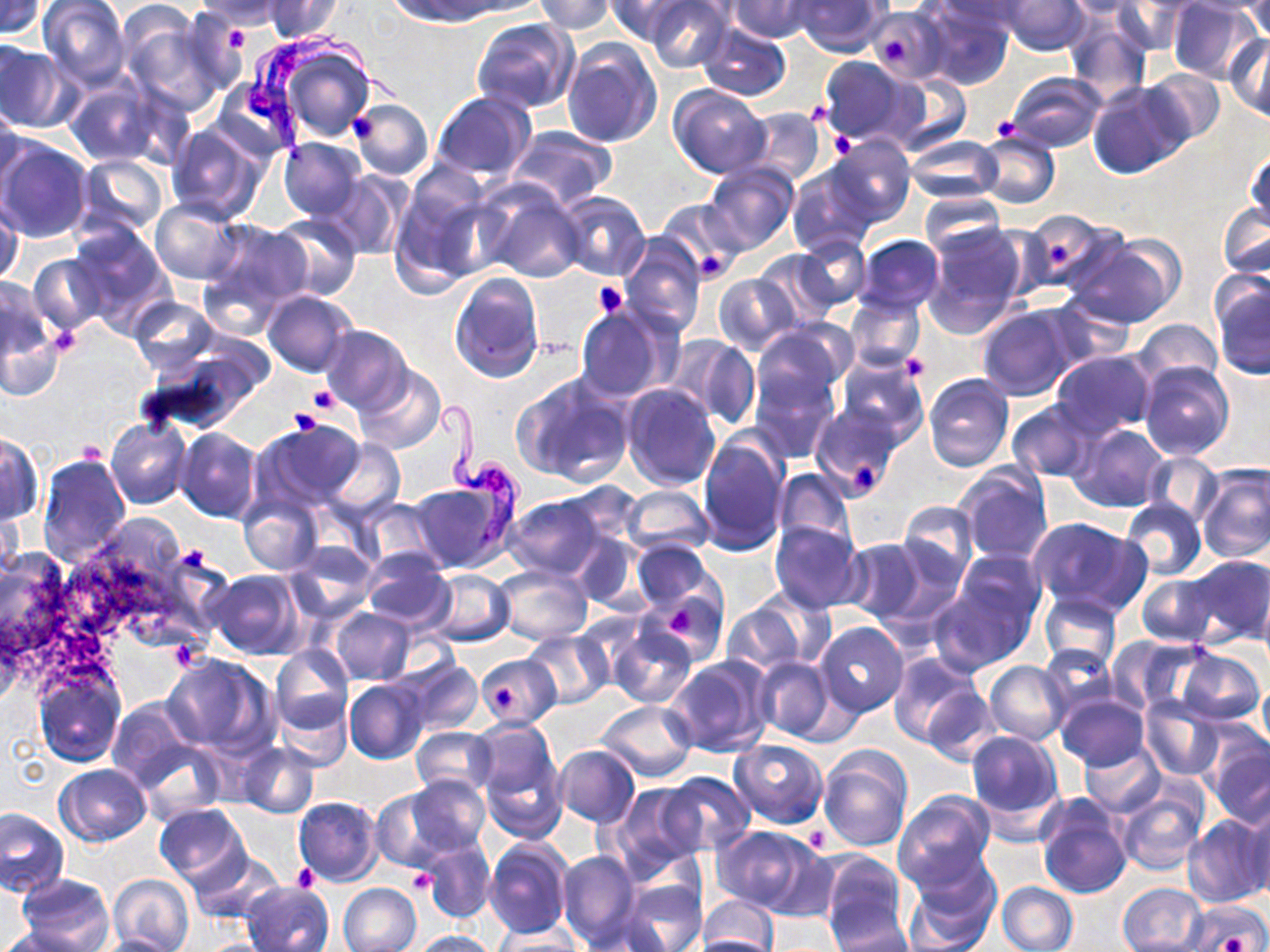

Summary:
  - Coordinate format: approximate bounding boxes as (x1, y1, x2, y2) in pixels
  - Platelet locations: (219, 20, 251, 51), (881, 34, 909, 66), (347, 111, 381, 143), (989, 116, 1021, 141), (829, 131, 857, 159), (1048, 243, 1072, 268), (696, 250, 729, 282), (593, 280, 629, 318), (48, 321, 85, 362), (902, 355, 930, 381), (307, 385, 342, 414), (288, 407, 323, 439), (77, 440, 104, 465), (853, 459, 885, 498), (178, 543, 211, 576), (665, 607, 699, 638), (495, 688, 517, 709), (801, 824, 832, 853), (292, 863, 320, 890), (407, 869, 437, 893), (1222, 932, 1247, 950)
  - Uninfected red blood cell locations: (0, 0, 49, 40), (38, 0, 130, 89), (264, 0, 344, 42), (453, 0, 547, 18), (534, 0, 617, 35), (605, 0, 693, 45), (644, 0, 733, 72), (730, 0, 818, 42), (794, 0, 888, 56), (933, 0, 1028, 38), (997, 0, 1090, 55), (1057, 0, 1149, 19), (1166, 0, 1265, 85), (1182, 0, 1270, 16), (1240, 0, 1270, 41), (191, 1, 290, 29), (392, 1, 499, 24), (1111, 1, 1189, 56), (116, 2, 207, 97), (918, 2, 1014, 90), (174, 8, 251, 96), (867, 9, 945, 82), (1062, 12, 1152, 103), (8, 16, 122, 123), (471, 18, 579, 113), (697, 22, 792, 100), (1226, 35, 1270, 122), (267, 39, 375, 143), (562, 39, 662, 148), (0, 42, 73, 131), (816, 55, 921, 148), (1139, 67, 1227, 147), (887, 72, 971, 156), (1006, 72, 1108, 153), (66, 76, 159, 167), (213, 77, 303, 163), (1087, 82, 1188, 180), (668, 83, 772, 178), (431, 91, 536, 184), (349, 99, 433, 179), (0, 106, 25, 195), (738, 107, 826, 185), (165, 122, 267, 226), (509, 126, 614, 208), (976, 132, 1059, 209), (826, 134, 914, 226), (0, 136, 92, 243), (905, 136, 1002, 204), (279, 137, 366, 221), (1245, 147, 1269, 233), (77, 155, 170, 236), (702, 163, 799, 255), (786, 167, 875, 256), (322, 171, 408, 259), (387, 180, 496, 293), (478, 180, 587, 283), (919, 189, 1006, 255), (556, 191, 651, 280), (0, 198, 22, 289), (150, 200, 241, 284), (657, 200, 745, 278), (1218, 201, 1269, 283), (1019, 210, 1122, 296), (270, 214, 360, 301), (201, 218, 312, 322), (67, 220, 174, 335), (921, 222, 1028, 336), (618, 234, 706, 336), (854, 234, 944, 315), (1068, 234, 1183, 329), (794, 235, 871, 312), (754, 249, 840, 326), (27, 252, 105, 337), (450, 272, 544, 381), (713, 273, 798, 355), (1210, 275, 1270, 380), (1, 278, 61, 382), (263, 290, 358, 377), (845, 294, 925, 373), (1044, 294, 1137, 369), (128, 297, 217, 374), (575, 305, 672, 403), (977, 305, 1078, 400), (1132, 319, 1222, 387), (321, 325, 413, 413), (750, 325, 850, 415), (668, 335, 758, 429), (135, 337, 272, 437), (834, 349, 928, 443), (1050, 350, 1157, 439), (1138, 362, 1234, 460), (750, 363, 838, 461), (356, 365, 446, 454), (923, 373, 1015, 472), (516, 374, 634, 487), (620, 383, 721, 491), (1006, 398, 1100, 483), (810, 404, 903, 501), (106, 417, 192, 511), (253, 419, 367, 512), (1069, 423, 1169, 513), (176, 427, 261, 522), (697, 431, 790, 555), (0, 433, 42, 525), (321, 437, 405, 521), (38, 452, 130, 564), (1141, 452, 1222, 528), (954, 463, 1052, 564), (1195, 465, 1270, 562), (773, 467, 854, 551), (409, 478, 513, 572), (620, 485, 713, 556), (237, 493, 321, 576), (501, 494, 612, 580), (0, 497, 25, 582), (356, 498, 444, 572), (1120, 498, 1206, 581), (896, 501, 977, 594), (1026, 517, 1149, 617), (54, 519, 220, 661), (768, 520, 867, 613), (842, 538, 933, 626), (629, 541, 719, 617), (287, 543, 378, 620), (359, 547, 453, 629), (0, 550, 74, 656), (1179, 556, 1270, 647), (932, 561, 1041, 672), (495, 565, 592, 643), (423, 569, 515, 647), (207, 570, 303, 659), (1136, 571, 1220, 646), (1257, 587, 1270, 673), (655, 592, 727, 662), (1039, 592, 1123, 674), (722, 600, 814, 675), (330, 607, 417, 686), (815, 622, 908, 717), (607, 626, 697, 707), (523, 631, 613, 709), (1108, 636, 1208, 713), (271, 645, 353, 732), (1038, 647, 1120, 719), (1173, 648, 1265, 726), (888, 651, 983, 749), (162, 654, 278, 757), (475, 654, 562, 729), (666, 656, 774, 759), (753, 657, 833, 741), (397, 659, 483, 738), (985, 661, 1071, 744), (33, 668, 126, 767), (1259, 678, 1270, 754), (345, 679, 428, 763), (922, 685, 1001, 766), (1054, 694, 1149, 770), (1139, 696, 1225, 783), (273, 698, 352, 772), (106, 700, 196, 790), (597, 701, 699, 781), (470, 717, 562, 809), (411, 727, 497, 798), (966, 730, 1065, 831), (1206, 737, 1270, 827), (728, 740, 829, 826), (135, 741, 224, 823), (1081, 741, 1165, 816), (238, 744, 320, 818), (818, 744, 913, 852), (553, 745, 640, 828), (482, 748, 569, 842), (54, 764, 152, 846), (660, 770, 755, 856), (403, 775, 491, 862), (609, 783, 703, 877), (370, 787, 469, 871), (893, 791, 996, 891), (1117, 791, 1208, 876), (1036, 794, 1133, 898), (293, 795, 383, 886), (154, 803, 249, 887), (1240, 804, 1270, 903), (1, 809, 69, 899), (1182, 814, 1270, 908), (713, 825, 821, 915), (484, 836, 573, 940), (419, 839, 497, 925), (189, 850, 286, 925), (557, 850, 640, 950), (817, 851, 910, 949), (902, 858, 1001, 952), (107, 873, 196, 952), (15, 874, 114, 951), (620, 879, 706, 952), (242, 881, 334, 952), (996, 881, 1076, 952), (1118, 881, 1208, 952), (339, 882, 421, 952), (698, 894, 780, 952), (1187, 900, 1270, 951), (826, 907, 913, 951), (579, 911, 672, 950), (0, 925, 102, 952), (491, 929, 584, 951), (409, 930, 499, 951), (88, 933, 184, 952), (695, 933, 779, 952), (194, 939, 279, 952)
  - Trypanosoma brucei locations: (245, 25, 405, 164), (432, 398, 526, 550)
  - Slide-level diagnosis: Trypanosoma brucei
  - Magnification: 1000x
  - Image size: 1270×952 pixels
  - Field of view: single
  - Preparation: thin blood film
  - Modality: optical microscopy
  - Stain: May-Grünwald-Giemsa